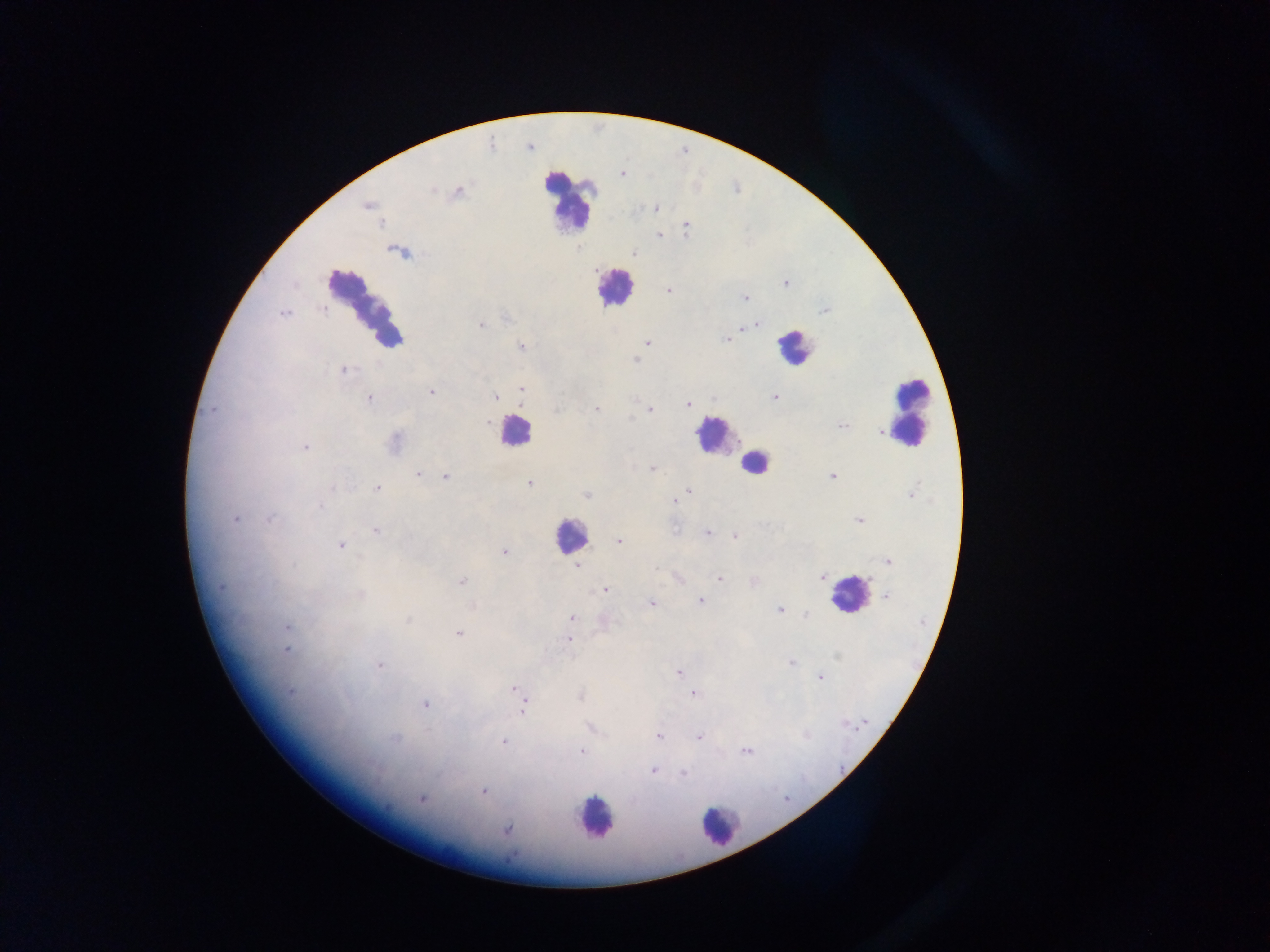
{
  "leukocyte_locations": "approximate centers as [x, y] in pixels: [568, 200], [614, 288], [365, 305], [793, 346], [909, 411], [514, 432], [713, 435], [754, 463], [569, 535], [849, 595], [595, 818], [719, 826]",
  "preparation": "thick blood film",
  "image_size": "1270×952 pixels",
  "country": "Ghana",
  "capture": "mobile-phone photograph through a microscope",
  "field_of_view": "single",
  "plasmodium_parasite_locations": "approximate centers as [x, y] in pixels: [621, 174], [431, 190], [458, 192], [367, 206], [656, 208], [685, 228], [659, 235], [634, 254], [785, 284], [668, 290], [745, 299], [322, 309], [825, 310], [284, 313], [756, 324], [480, 325], [750, 326], [743, 327], [727, 339], [648, 342], [521, 346], [635, 360], [344, 370], [521, 389], [431, 392], [495, 396], [774, 397], [369, 399], [713, 399], [688, 405], [212, 410], [596, 410], [649, 410], [487, 421], [843, 426], [881, 432], [395, 441], [305, 447], [652, 468], [418, 475], [446, 477], [832, 477], [529, 483], [378, 488], [688, 491], [913, 492], [586, 494], [675, 501], [320, 506], [236, 519], [269, 519], [859, 520], [376, 531], [707, 532], [735, 537], [619, 541], [340, 546], [504, 553], [888, 561], [577, 566], [657, 568], [822, 576], [678, 579], [719, 579], [753, 580], [462, 581], [220, 588], [605, 589], [360, 594], [886, 596], [701, 601], [651, 604], [779, 609], [805, 614], [571, 617], [408, 619], [287, 626], [458, 634], [568, 640], [286, 651], [791, 663], [380, 665], [678, 672], [820, 677], [514, 688], [291, 692], [693, 693], [580, 696], [426, 704], [523, 707], [658, 736], [699, 737], [395, 738], [504, 742], [581, 751], [745, 751], [653, 771], [683, 772], [483, 792], [421, 799], [507, 830]"
}